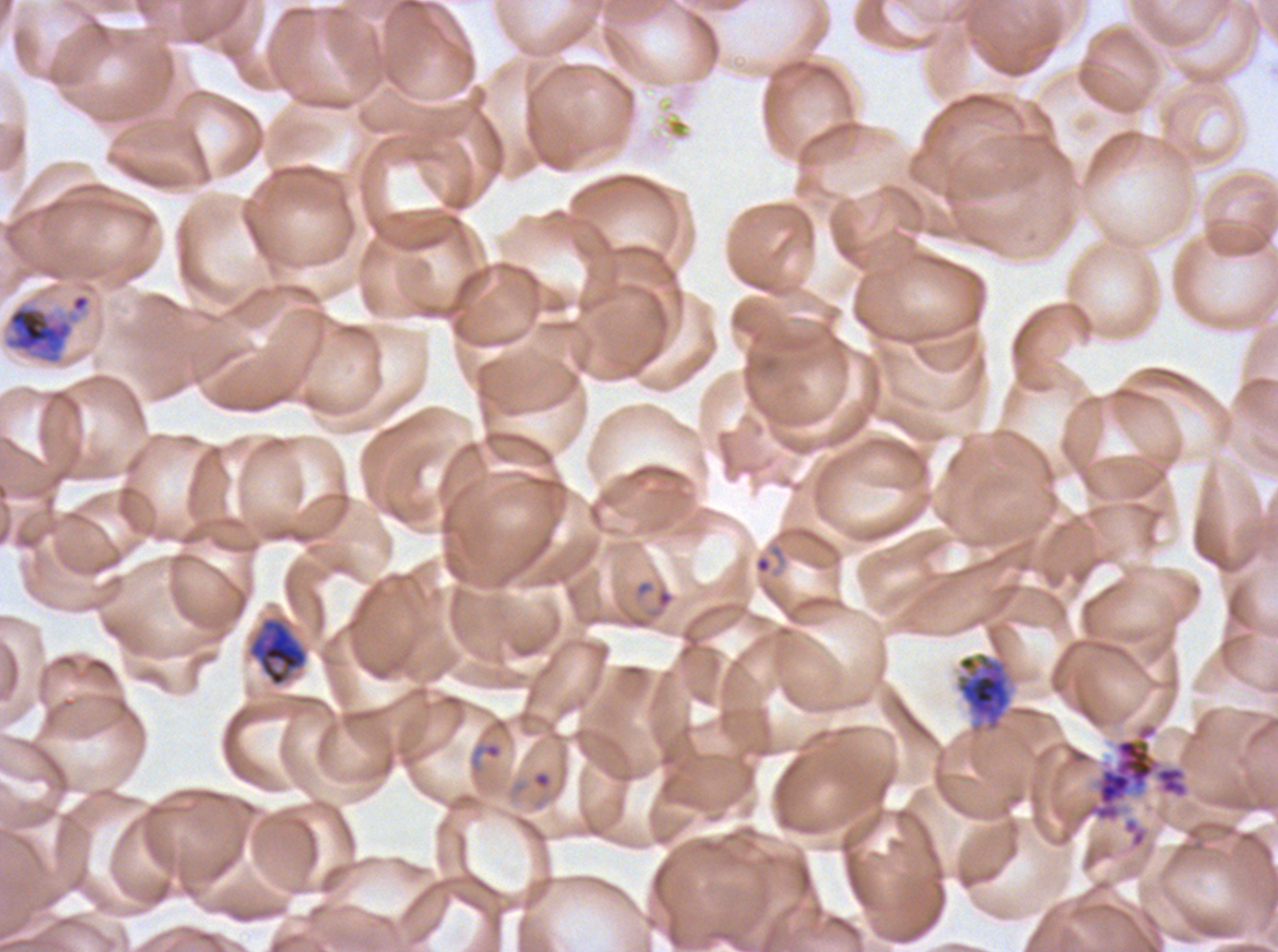

notation = approximate bounding rectangles given as corner coordinates in pixels from the top-left
segmenter locations = (x1=1073, y1=721, x2=1190, y2=825)
ring locations = (x1=646, y1=585, x2=675, y2=620), (x1=470, y1=740, x2=503, y2=774), (x1=535, y1=773, x2=549, y2=787)
early schizont locations = (x1=2, y1=292, x2=92, y2=366), (x1=955, y1=652, x2=1013, y2=734)
late trophozoite locations = (x1=248, y1=617, x2=308, y2=687)
specimen = Plasmodium falciparum from a patient in The Gambia, cultured ex vivo for 24 to 48 hours
life-cycle stages observed = ring, late trophozoite, early schizont, segmenter
field of view = one sub-image of a larger composite
preparation = thin blood film
stain = Giemsa
image size = 1278×952 pixels